Identify the cell.
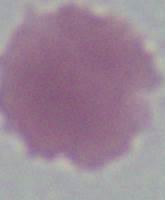
This is an erythrocyte.

Summary:
  - Modality: photomicrograph
  - Magnification: 1000x